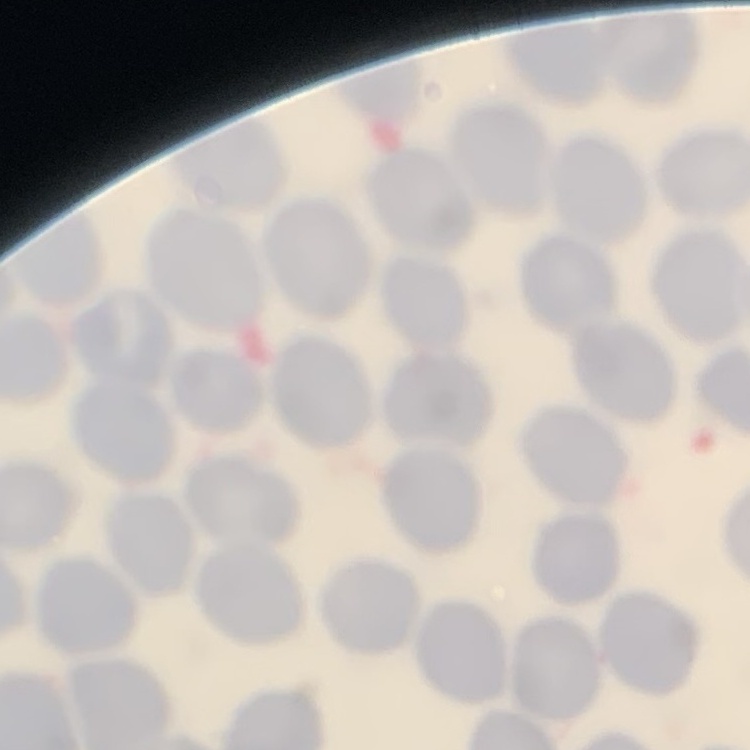
The erythrocytes exhibit no rouleaux formation. Stained with either Field's or Giemsa. Square crop of a larger photomicrograph. Thin blood film.